Classify this cell by malaria status.
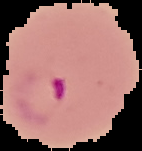

It is parasitized.

preparation: thin blood film
image_size: 142×151 pixels
image_type: segmented cell region with the area outside set to black